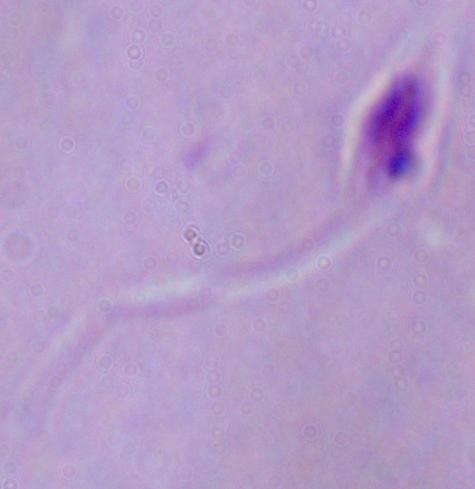
Photomicrograph. A Leishmania parasite is seen. 1000x magnification.